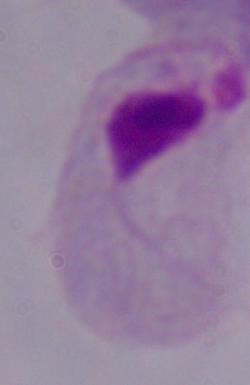

{
  "identification": "trichomonad",
  "magnification": "1000x",
  "modality": "micrograph"
}